Name the blood parasite species.
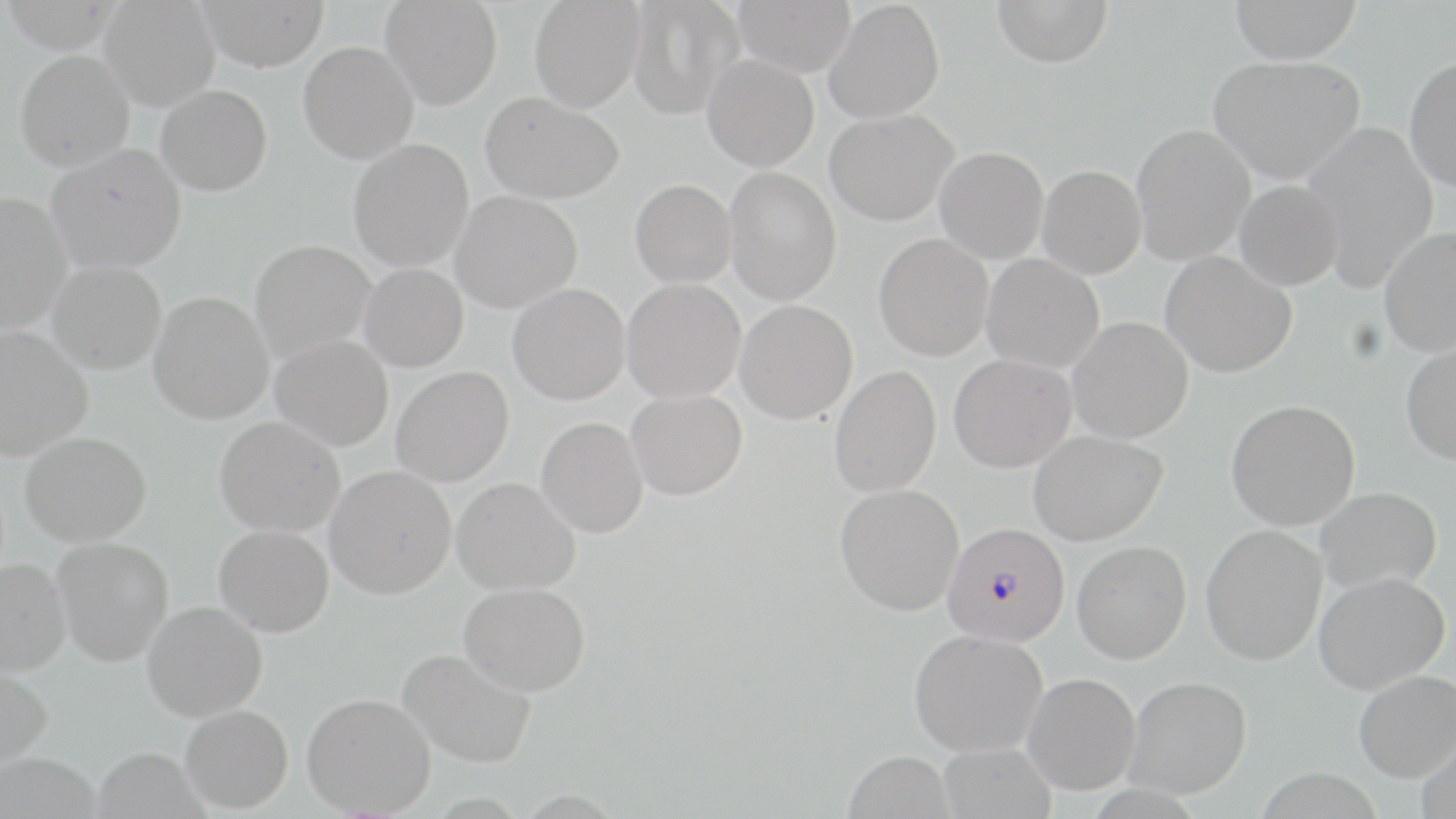
Plasmodium falciparum.

uninfected red blood cell locations = approximate bounding boxes as (x1, y1, x2, y2) in pixels: (100, 0, 220, 111), (196, 0, 330, 72), (381, 0, 502, 110), (529, 0, 645, 112), (627, 0, 744, 119), (733, 0, 856, 76), (992, 0, 1113, 68), (1229, 0, 1361, 65), (824, 1, 945, 123), (298, 41, 418, 164), (14, 50, 134, 171), (702, 54, 819, 172), (1207, 55, 1367, 186), (1404, 56, 1456, 193), (155, 84, 272, 196), (480, 90, 623, 204), (825, 109, 958, 225), (1301, 122, 1439, 292), (1131, 124, 1256, 266), (348, 139, 474, 271), (46, 144, 186, 274), (935, 147, 1048, 264), (1038, 165, 1146, 279), (724, 166, 841, 305), (630, 179, 736, 287), (1234, 180, 1344, 291), (450, 190, 582, 313), (0, 191, 72, 332), (1379, 225, 1456, 358), (874, 233, 994, 360), (249, 239, 376, 364), (1161, 251, 1298, 378), (981, 254, 1105, 373), (47, 260, 166, 374), (359, 263, 468, 371), (622, 278, 746, 403), (508, 283, 630, 405), (148, 291, 274, 424), (735, 299, 858, 424), (1066, 317, 1193, 443), (0, 325, 93, 460), (270, 334, 393, 451), (1401, 341, 1456, 465), (949, 353, 1076, 473), (828, 365, 941, 497), (391, 366, 513, 487), (626, 389, 747, 501), (1226, 399, 1360, 530), (215, 416, 345, 537), (536, 417, 649, 538), (1028, 430, 1168, 546), (20, 431, 151, 546), (324, 465, 456, 598), (451, 477, 580, 595), (834, 483, 964, 615), (1314, 487, 1442, 593), (214, 524, 333, 637), (1201, 525, 1328, 665), (52, 537, 174, 667), (1072, 540, 1192, 664), (0, 557, 71, 675), (1313, 571, 1451, 695), (459, 582, 590, 696), (142, 600, 267, 721), (908, 628, 1048, 756), (397, 647, 537, 768), (0, 664, 53, 770), (1353, 669, 1456, 782), (1023, 672, 1141, 794), (1124, 676, 1252, 798), (302, 692, 436, 816), (180, 704, 293, 813), (1415, 732, 1456, 817), (937, 742, 1055, 819), (1, 745, 107, 819), (95, 747, 224, 819), (843, 750, 956, 819)
image size = 1456×819 pixels
Plasmodium falciparum-infected red blood cell locations = approximate bounding boxes as (x1, y1, x2, y2) in pixels: (942, 522, 1070, 646)
preparation = thin blood smear
magnification = 1000x
field of view = one of a larger specimen
modality = optical microscopy
stain = May-Grünwald-Giemsa